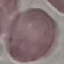

Summary:
  - Result: negative for malaria parasites
  - Preparation: thin smear
  - Capture: smartphone camera at the microscope eyepiece
  - Stain: Giemsa
  - Image type: automatically extracted cell patch, resized to 64 × 64 pixels